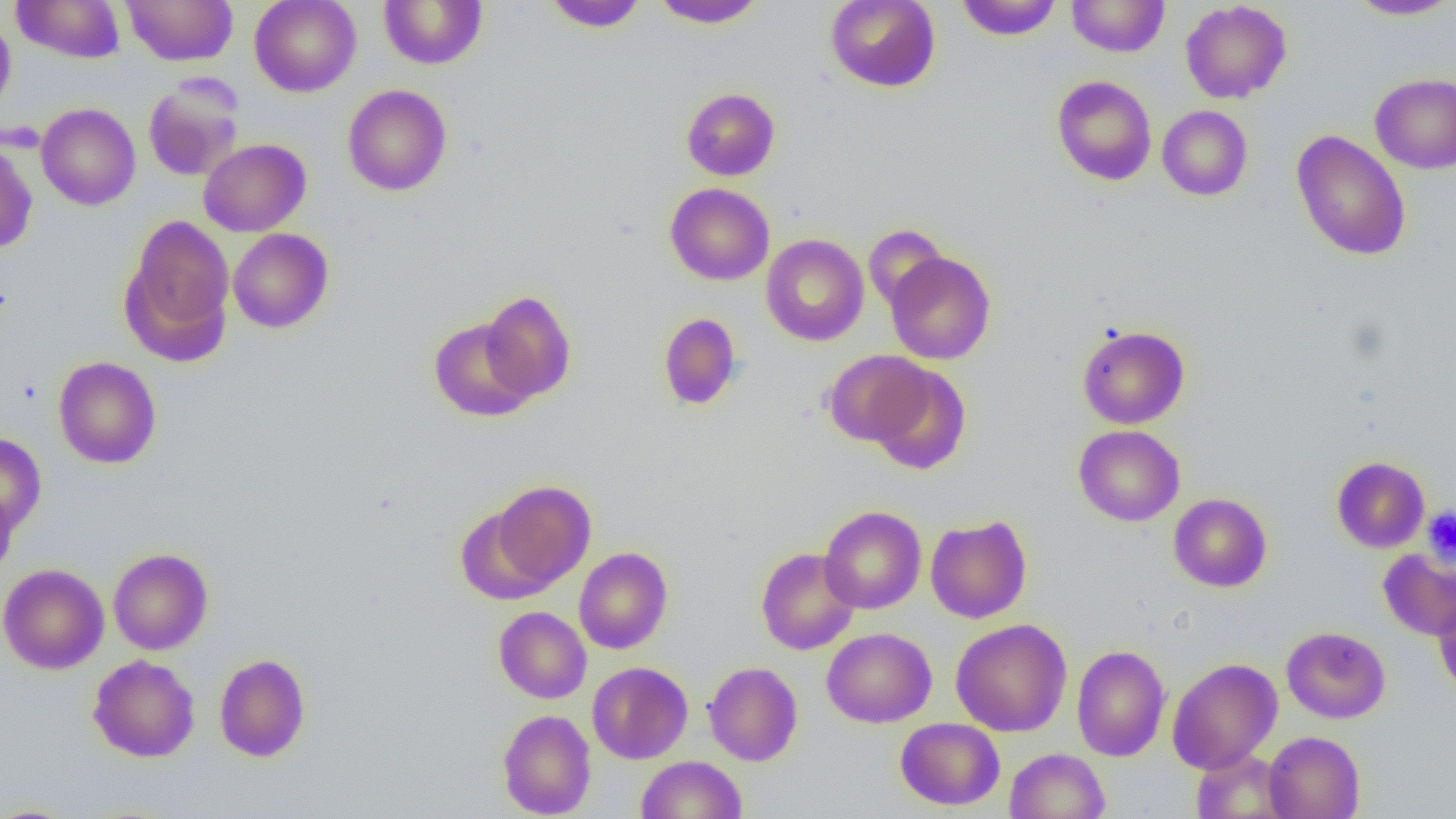

Summary:
  - Coordinate format: approximate bounding boxes as named x1/y1/x2/y2 corners in pixels
  - Uninfected red blood cell locations: (x1=12, y1=0, x2=126, y2=63), (x1=121, y1=0, x2=238, y2=66), (x1=249, y1=0, x2=361, y2=97), (x1=378, y1=0, x2=487, y2=69), (x1=542, y1=0, x2=648, y2=32), (x1=652, y1=0, x2=767, y2=29), (x1=825, y1=0, x2=940, y2=92), (x1=956, y1=0, x2=1063, y2=41), (x1=1067, y1=0, x2=1169, y2=57), (x1=1345, y1=0, x2=1456, y2=20), (x1=1180, y1=1, x2=1292, y2=103), (x1=0, y1=15, x2=16, y2=118), (x1=1370, y1=73, x2=1456, y2=174), (x1=1052, y1=75, x2=1157, y2=186), (x1=142, y1=78, x2=244, y2=182), (x1=342, y1=84, x2=452, y2=196), (x1=681, y1=87, x2=780, y2=181), (x1=36, y1=103, x2=140, y2=210), (x1=1157, y1=105, x2=1252, y2=200), (x1=1291, y1=130, x2=1411, y2=261), (x1=198, y1=138, x2=311, y2=237), (x1=0, y1=140, x2=37, y2=255), (x1=664, y1=183, x2=775, y2=285), (x1=122, y1=215, x2=236, y2=362), (x1=864, y1=224, x2=949, y2=313), (x1=228, y1=228, x2=333, y2=333), (x1=761, y1=234, x2=869, y2=346), (x1=885, y1=252, x2=995, y2=364), (x1=479, y1=290, x2=577, y2=403), (x1=657, y1=312, x2=743, y2=411), (x1=428, y1=318, x2=538, y2=422), (x1=1077, y1=325, x2=1190, y2=429), (x1=822, y1=350, x2=932, y2=447), (x1=53, y1=356, x2=161, y2=469), (x1=867, y1=362, x2=972, y2=475), (x1=1073, y1=425, x2=1185, y2=526), (x1=0, y1=433, x2=47, y2=534), (x1=1331, y1=456, x2=1430, y2=553), (x1=487, y1=480, x2=597, y2=591), (x1=0, y1=488, x2=18, y2=580), (x1=1168, y1=492, x2=1272, y2=592), (x1=819, y1=506, x2=926, y2=614), (x1=925, y1=516, x2=1032, y2=623), (x1=573, y1=547, x2=673, y2=654), (x1=755, y1=547, x2=861, y2=655), (x1=108, y1=548, x2=213, y2=655), (x1=1379, y1=548, x2=1456, y2=640), (x1=0, y1=563, x2=109, y2=674), (x1=1432, y1=590, x2=1456, y2=698), (x1=494, y1=606, x2=591, y2=703), (x1=951, y1=619, x2=1072, y2=736), (x1=1281, y1=626, x2=1391, y2=723), (x1=821, y1=627, x2=937, y2=728), (x1=1071, y1=644, x2=1171, y2=761), (x1=88, y1=654, x2=200, y2=762), (x1=214, y1=654, x2=311, y2=762), (x1=1167, y1=657, x2=1282, y2=774), (x1=587, y1=661, x2=693, y2=764), (x1=703, y1=661, x2=803, y2=765), (x1=497, y1=709, x2=596, y2=818), (x1=896, y1=718, x2=1005, y2=811), (x1=1263, y1=731, x2=1365, y2=819), (x1=1005, y1=747, x2=1109, y2=819), (x1=1191, y1=749, x2=1291, y2=818), (x1=635, y1=755, x2=747, y2=819), (x1=0, y1=803, x2=80, y2=817)
  - Platelet locations: (x1=1422, y1=507, x2=1456, y2=565)
  - Slide-level diagnosis: negative for blood parasites
  - Image size: 1456×819 pixels
  - Magnification: 1000x
  - Preparation: thin blood film
  - Modality: optical microscopy
  - Field of view: one of a larger specimen